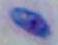
Micrograph. Captured at 1000x magnification. Toxoplasma gondii is seen.